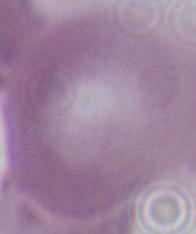

1000x magnification. Photomicrograph. An erythrocyte is seen.